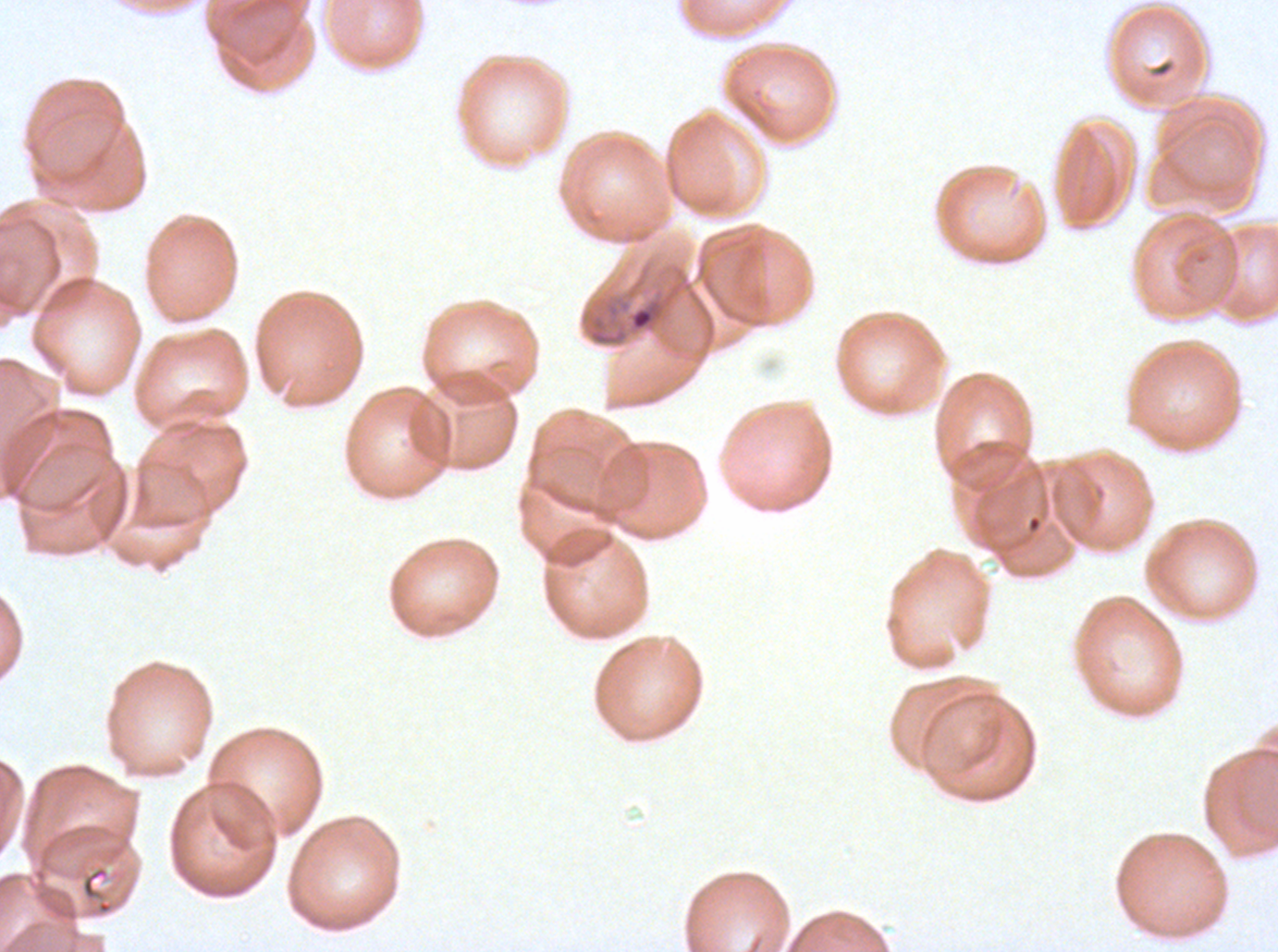

specimen: ex-vivo P. falciparum culture from a patient in The Gambia, grown for 24 to 48 hours
preparation: thin blood film
field_of_view: sub-image separated from a larger composite
image_size: 1278×952 pixels
stain: Giemsa
debris_locations: 'approximate bounding boxes as (x1, y1, x2, y2) in pixels: (1026, 515, 1041, 532), (80, 865, 114, 915)'
late_ring_early_trophozoite_locations: 'approximate bounding boxes as (x1, y1, x2, y2) in pixels: (631, 308, 654, 330)'